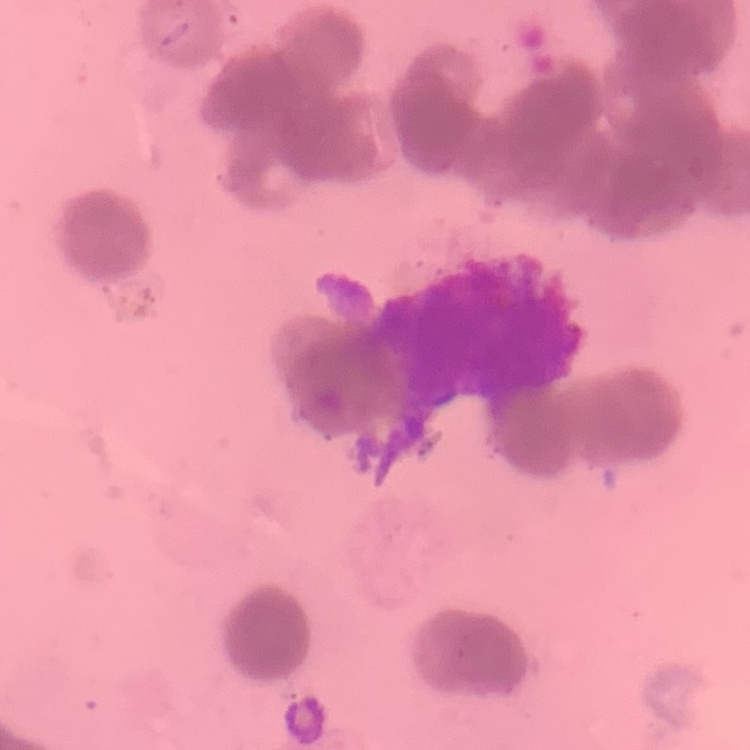

The erythrocytes exhibit rouleaux formation. Field's or Giemsa stain. Thin blood smear. One tile cut from a larger photomicrograph.